Outline each white blood cell.
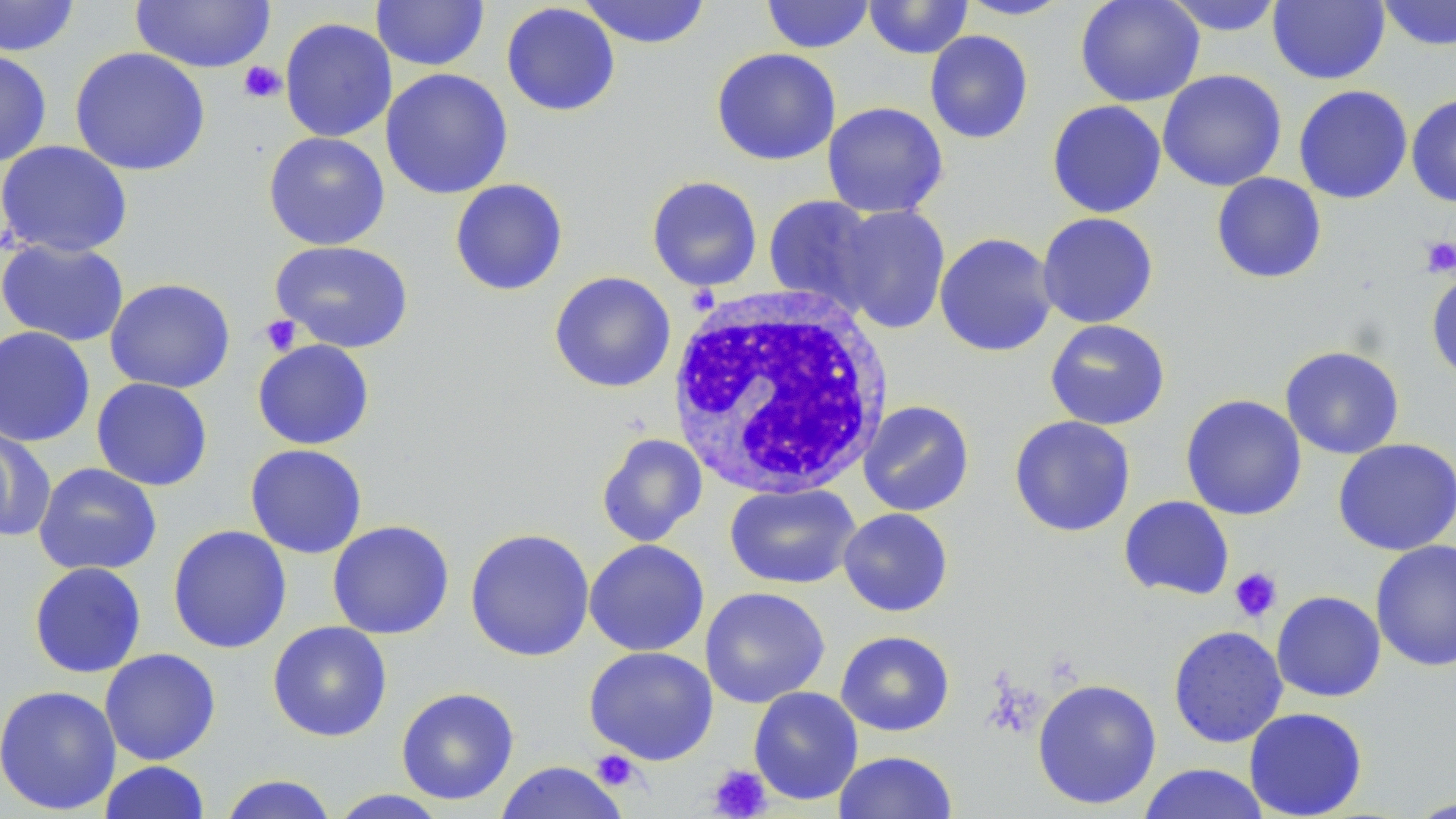
Approximate bounding boxes as (x1, y1, x2, y2) in pixels.
White blood cells: (666, 286, 895, 499).

slide-level diagnosis = negative for blood parasites
modality = optical microscopy
image size = 1456×819 pixels
magnification = 1000x
uninfected red blood cell locations = approximate bounding boxes as (x1, y1, x2, y2) in pixels: (0, 0, 80, 57), (578, 0, 711, 49), (761, 0, 874, 54), (864, 0, 973, 60), (958, 0, 1073, 20), (1074, 0, 1206, 107), (1160, 0, 1287, 36), (1268, 0, 1389, 85), (1377, 0, 1456, 51), (131, 1, 275, 73), (371, 1, 489, 71), (501, 2, 621, 116), (279, 17, 397, 143), (925, 30, 1034, 144), (69, 46, 211, 177), (711, 47, 841, 166), (0, 48, 52, 167), (380, 68, 513, 199), (1157, 69, 1287, 192), (1293, 85, 1413, 204), (1406, 93, 1456, 207), (1046, 100, 1166, 218), (822, 101, 948, 219), (263, 131, 390, 250), (0, 140, 133, 259), (1211, 172, 1327, 284), (646, 175, 762, 292), (449, 179, 568, 296), (762, 195, 883, 312), (833, 204, 951, 334), (1037, 212, 1159, 328), (934, 232, 1058, 357), (0, 238, 130, 347), (270, 240, 414, 353), (1426, 269, 1456, 386), (549, 271, 676, 393), (104, 278, 235, 394), (1045, 319, 1171, 431), (0, 325, 96, 448), (252, 339, 375, 450), (1280, 345, 1405, 459), (91, 377, 213, 491), (1180, 394, 1307, 520), (858, 400, 975, 517), (1009, 415, 1136, 537), (0, 426, 55, 543), (596, 433, 708, 547), (1334, 438, 1455, 555), (245, 444, 368, 559), (33, 462, 162, 577), (724, 483, 861, 589), (1119, 495, 1234, 600), (838, 508, 954, 617), (327, 520, 454, 639), (168, 525, 291, 654), (465, 528, 595, 662), (584, 539, 709, 657), (1370, 539, 1456, 672), (29, 562, 146, 679), (700, 586, 830, 708), (1271, 590, 1386, 702), (267, 621, 392, 742), (1168, 625, 1288, 748), (835, 630, 955, 736), (584, 646, 718, 765), (99, 648, 220, 765), (1032, 678, 1162, 810), (0, 684, 122, 815), (749, 686, 863, 805), (395, 687, 519, 805), (1244, 707, 1368, 818), (833, 751, 957, 818), (98, 760, 211, 819), (493, 761, 630, 819), (1137, 762, 1271, 819), (219, 774, 337, 819), (327, 789, 450, 818), (1405, 796, 1456, 818)
platelet locations = approximate bounding boxes as (x1, y1, x2, y2) in pixels: (238, 60, 286, 104), (1421, 236, 1456, 278), (259, 314, 303, 356), (1229, 567, 1282, 623), (592, 750, 642, 791), (707, 765, 771, 818)
field of view = one of a larger specimen
preparation = thin blood smear
stain = May-Grünwald-Giemsa